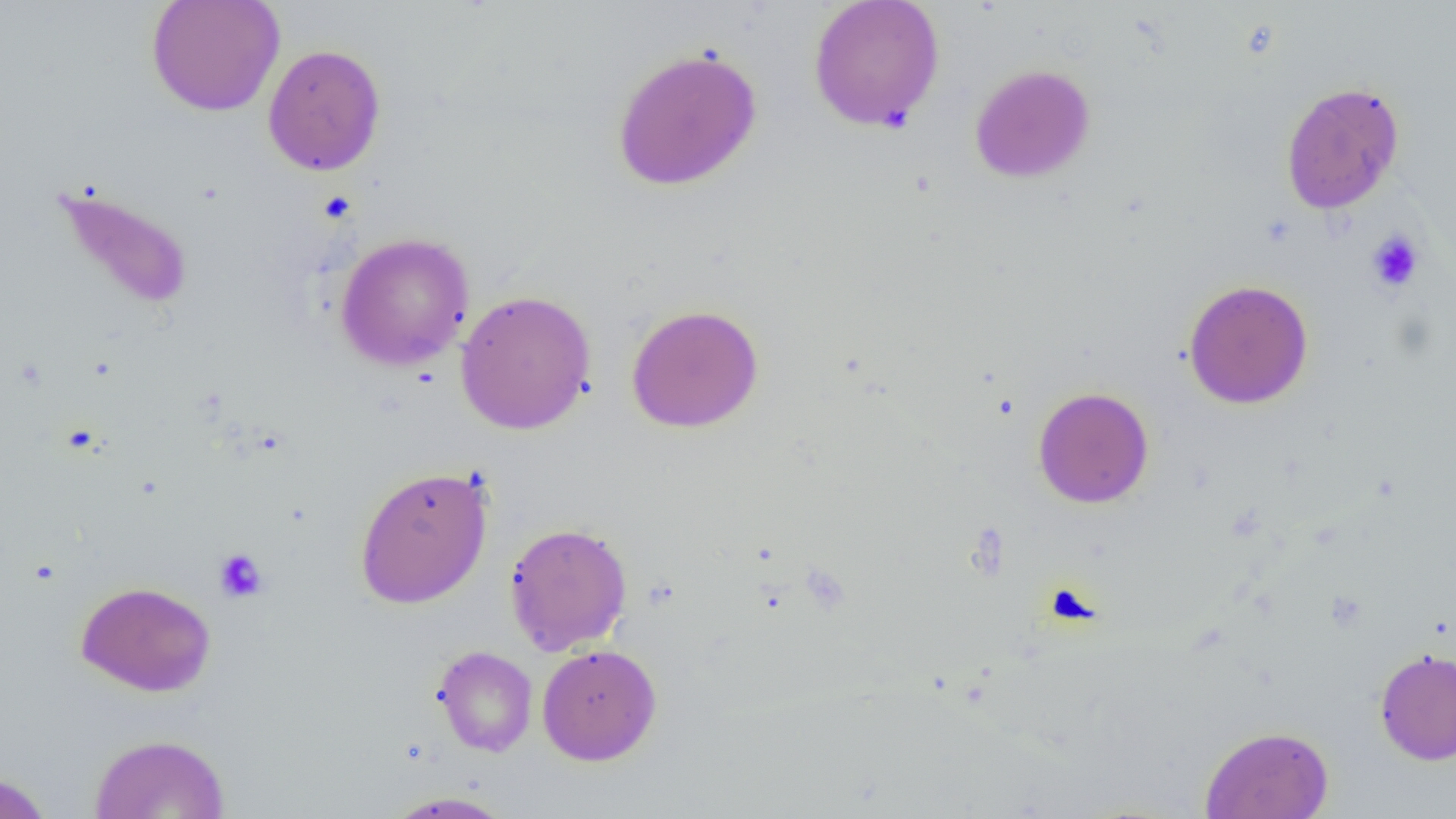

Summary:
  - Coordinate format: approximate bounding boxes as named x1/y1/x2/y2 corners in pixels
  - Uninfected red blood cell locations: (x1=146, y1=0, x2=285, y2=116), (x1=808, y1=0, x2=945, y2=132), (x1=263, y1=43, x2=386, y2=176), (x1=611, y1=46, x2=763, y2=191), (x1=969, y1=63, x2=1095, y2=183), (x1=1280, y1=80, x2=1405, y2=215), (x1=50, y1=182, x2=194, y2=312), (x1=335, y1=232, x2=474, y2=372), (x1=1183, y1=279, x2=1314, y2=409), (x1=456, y1=289, x2=596, y2=435), (x1=625, y1=304, x2=764, y2=433), (x1=1033, y1=386, x2=1154, y2=508), (x1=354, y1=465, x2=494, y2=608), (x1=503, y1=521, x2=632, y2=656), (x1=76, y1=580, x2=216, y2=697), (x1=537, y1=644, x2=662, y2=766), (x1=431, y1=645, x2=538, y2=757), (x1=1375, y1=647, x2=1456, y2=765), (x1=1200, y1=725, x2=1334, y2=819), (x1=89, y1=733, x2=232, y2=818), (x1=0, y1=771, x2=54, y2=819), (x1=381, y1=791, x2=515, y2=818)
  - Platelet locations: (x1=1367, y1=230, x2=1424, y2=293), (x1=214, y1=548, x2=268, y2=603)
  - Slide-level diagnosis: negative for blood parasites
  - Field of view: one of a larger specimen
  - Magnification: 1000x
  - Preparation: thin blood film
  - Image size: 1456×819 pixels
  - Modality: optical microscopy